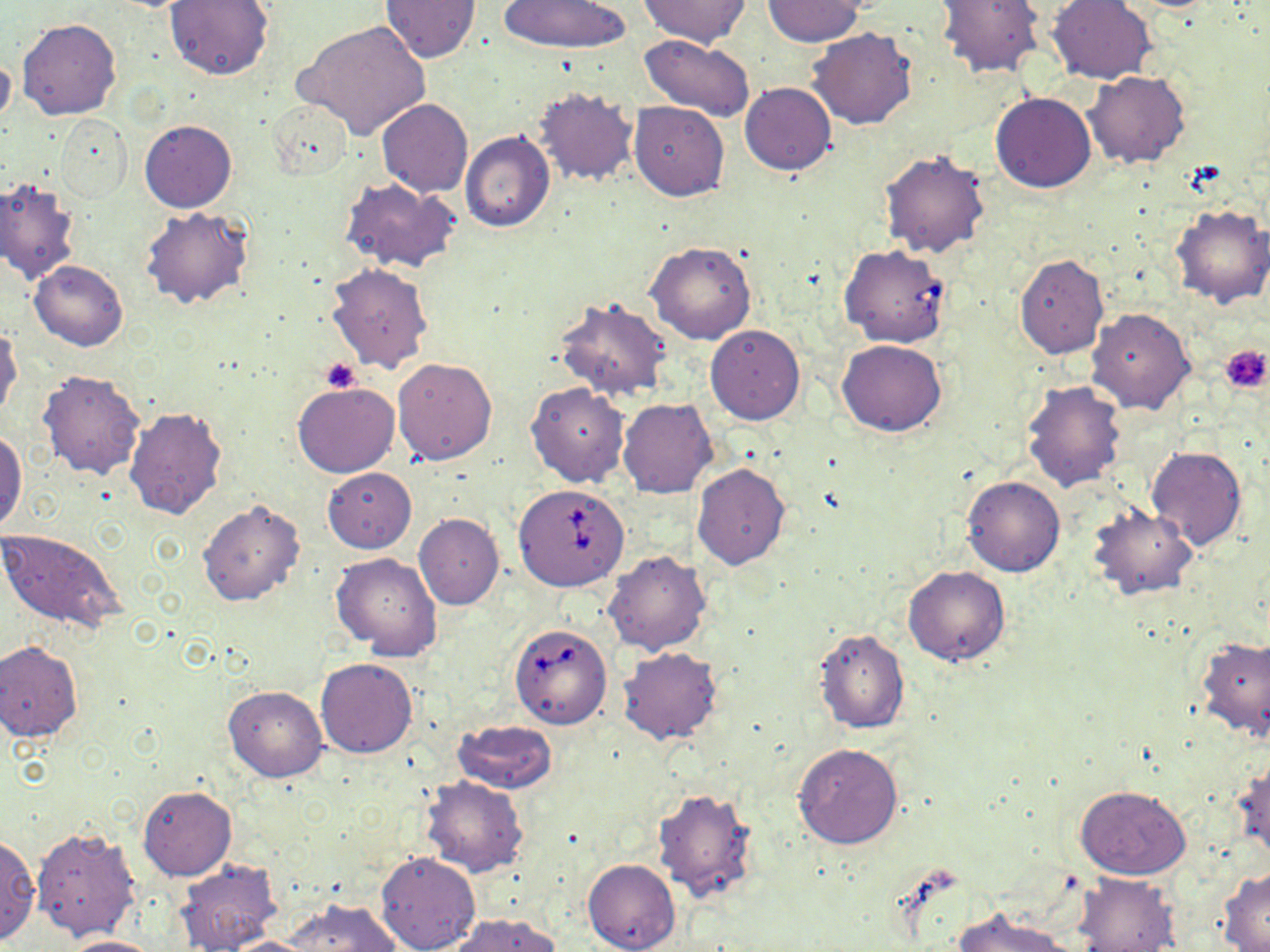

Summary:
  - Coordinate format: approximate bounding boxes as [x1, y1, x2, y2] in pixels
  - Platelet locations: [1220, 344, 1269, 393], [319, 357, 362, 394]
  - Uninfected red blood cell locations: [640, 0, 748, 47], [937, 0, 1045, 78], [1047, 0, 1156, 83], [164, 1, 273, 80], [380, 1, 481, 62], [497, 1, 629, 53], [762, 1, 868, 46], [17, 18, 122, 120], [296, 20, 430, 140], [807, 27, 917, 128], [640, 35, 756, 122], [0, 52, 16, 131], [1084, 71, 1190, 169], [740, 82, 837, 176], [531, 84, 639, 187], [991, 92, 1097, 193], [267, 99, 353, 181], [376, 99, 473, 197], [630, 102, 728, 201], [57, 115, 131, 203], [139, 120, 236, 212], [460, 131, 555, 232], [879, 146, 990, 257], [0, 179, 80, 285], [340, 179, 463, 273], [1168, 205, 1270, 309], [141, 208, 254, 310], [646, 241, 757, 344], [1013, 255, 1109, 358], [29, 259, 128, 351], [325, 262, 434, 373], [553, 296, 672, 400], [1086, 307, 1194, 415], [0, 324, 21, 420], [705, 325, 805, 424], [837, 339, 948, 436], [392, 358, 498, 465], [36, 369, 146, 481], [1021, 379, 1128, 494], [526, 382, 630, 488], [293, 383, 399, 477], [619, 398, 717, 498], [123, 407, 228, 521], [0, 431, 25, 532], [1146, 445, 1248, 551], [693, 462, 790, 569], [323, 468, 416, 552], [961, 474, 1066, 577], [196, 497, 305, 607], [1086, 503, 1199, 600], [414, 514, 503, 609], [0, 528, 126, 635], [603, 550, 712, 655], [331, 553, 442, 661], [903, 565, 1011, 666], [813, 628, 909, 734], [1196, 635, 1270, 742], [0, 641, 84, 742], [617, 646, 724, 747], [315, 658, 419, 759], [225, 686, 327, 782], [450, 719, 557, 794], [794, 744, 903, 849], [1232, 757, 1270, 862], [420, 776, 528, 877], [1075, 784, 1191, 880], [137, 785, 235, 881], [652, 786, 760, 906], [32, 826, 142, 940], [0, 834, 39, 944], [374, 850, 482, 952], [582, 858, 680, 952], [175, 859, 281, 951], [1217, 868, 1270, 951], [1073, 872, 1181, 951], [286, 899, 400, 952], [952, 907, 1070, 952], [449, 913, 559, 952], [58, 935, 164, 952], [220, 936, 321, 952]
  - Babesia divergens-infected red blood cell locations: [839, 244, 952, 348], [513, 484, 628, 591], [510, 621, 614, 730]
  - Slide-level diagnosis: Babesia divergens
  - Stain: May-Grünwald-Giemsa
  - Preparation: thin blood film
  - Image size: 1270×952 pixels
  - Modality: optical microscopy
  - Magnification: 1000x
  - Field of view: single